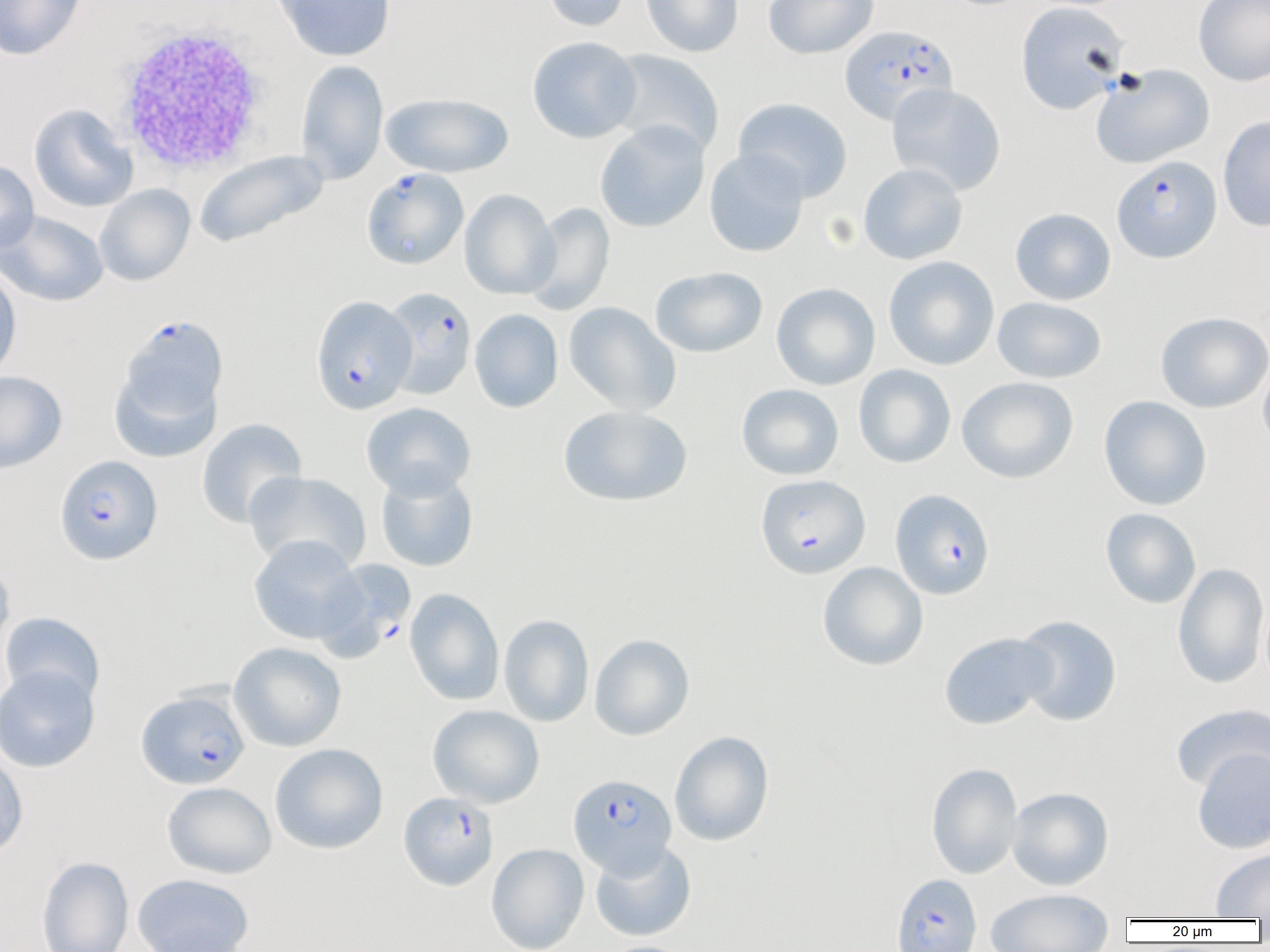

Summary:
  - Coordinate format: approximate bounding boxes as named x1/y1/x2/y2 corners in pixels
  - Uninfected red blood cell locations (subset): (x1=0, y1=0, x2=86, y2=60), (x1=272, y1=0, x2=396, y2=61), (x1=541, y1=0, x2=631, y2=32), (x1=641, y1=0, x2=744, y2=57), (x1=763, y1=0, x2=879, y2=60), (x1=1193, y1=0, x2=1270, y2=86), (x1=1016, y1=1, x2=1129, y2=115), (x1=527, y1=36, x2=642, y2=143), (x1=604, y1=49, x2=725, y2=157), (x1=295, y1=59, x2=388, y2=184), (x1=1090, y1=64, x2=1215, y2=169), (x1=886, y1=83, x2=1007, y2=196), (x1=380, y1=92, x2=513, y2=178), (x1=733, y1=97, x2=853, y2=201), (x1=28, y1=104, x2=137, y2=213), (x1=1218, y1=114, x2=1270, y2=233), (x1=594, y1=121, x2=710, y2=233), (x1=704, y1=148, x2=809, y2=258), (x1=193, y1=149, x2=329, y2=250), (x1=0, y1=159, x2=39, y2=254), (x1=858, y1=162, x2=968, y2=265), (x1=95, y1=183, x2=195, y2=286), (x1=459, y1=189, x2=559, y2=299), (x1=524, y1=203, x2=616, y2=315), (x1=1010, y1=208, x2=1116, y2=305), (x1=0, y1=210, x2=109, y2=307), (x1=883, y1=256, x2=999, y2=370), (x1=0, y1=264, x2=22, y2=382), (x1=650, y1=266, x2=768, y2=358), (x1=771, y1=282, x2=880, y2=390), (x1=992, y1=296, x2=1107, y2=384), (x1=563, y1=302, x2=681, y2=416), (x1=469, y1=309, x2=563, y2=413), (x1=1155, y1=311, x2=1270, y2=413), (x1=1258, y1=357, x2=1270, y2=453), (x1=108, y1=359, x2=223, y2=463), (x1=853, y1=364, x2=956, y2=468), (x1=0, y1=370, x2=67, y2=474), (x1=956, y1=376, x2=1079, y2=484), (x1=736, y1=383, x2=844, y2=481), (x1=1099, y1=395, x2=1212, y2=511), (x1=361, y1=402, x2=476, y2=499), (x1=558, y1=405, x2=692, y2=507), (x1=196, y1=418, x2=307, y2=529), (x1=375, y1=468, x2=478, y2=572), (x1=244, y1=470, x2=371, y2=573), (x1=1100, y1=508, x2=1201, y2=608), (x1=248, y1=535, x2=366, y2=644), (x1=0, y1=557, x2=14, y2=657), (x1=818, y1=562, x2=928, y2=671), (x1=1172, y1=562, x2=1269, y2=689), (x1=404, y1=588, x2=504, y2=705), (x1=1, y1=612, x2=106, y2=705), (x1=498, y1=614, x2=594, y2=727), (x1=1013, y1=615, x2=1122, y2=726), (x1=939, y1=632, x2=1056, y2=730), (x1=590, y1=634, x2=694, y2=740), (x1=229, y1=641, x2=346, y2=752), (x1=0, y1=664, x2=100, y2=773), (x1=1170, y1=703, x2=1270, y2=794), (x1=427, y1=704, x2=545, y2=808), (x1=669, y1=730, x2=774, y2=847), (x1=269, y1=743, x2=389, y2=854), (x1=1192, y1=748, x2=1270, y2=854), (x1=0, y1=749, x2=29, y2=864), (x1=926, y1=762, x2=1023, y2=879), (x1=162, y1=782, x2=277, y2=879), (x1=1007, y1=787, x2=1114, y2=890), (x1=590, y1=841, x2=696, y2=941), (x1=487, y1=844, x2=589, y2=952), (x1=1210, y1=847, x2=1270, y2=919), (x1=36, y1=856, x2=134, y2=952), (x1=132, y1=873, x2=254, y2=952), (x1=986, y1=888, x2=1114, y2=951)
  - White blood cell locations: (x1=113, y1=23, x2=275, y2=177)
  - Plasmodium falciparum-infected red blood cell locations (subset): (x1=840, y1=25, x2=958, y2=125), (x1=1112, y1=155, x2=1222, y2=263), (x1=361, y1=167, x2=468, y2=270), (x1=311, y1=295, x2=416, y2=414), (x1=117, y1=314, x2=229, y2=430), (x1=54, y1=455, x2=163, y2=565), (x1=756, y1=474, x2=870, y2=578), (x1=890, y1=488, x2=995, y2=600), (x1=315, y1=559, x2=416, y2=660), (x1=137, y1=688, x2=250, y2=789), (x1=569, y1=774, x2=676, y2=878), (x1=398, y1=791, x2=498, y2=890), (x1=892, y1=873, x2=981, y2=952)
  - Slide-level diagnosis: Plasmodium falciparum
  - Modality: light microscopy
  - Magnification: 1000x
  - Field of view: one of a larger specimen
  - Image size: 1270×952 pixels
  - Preparation: thin blood smear